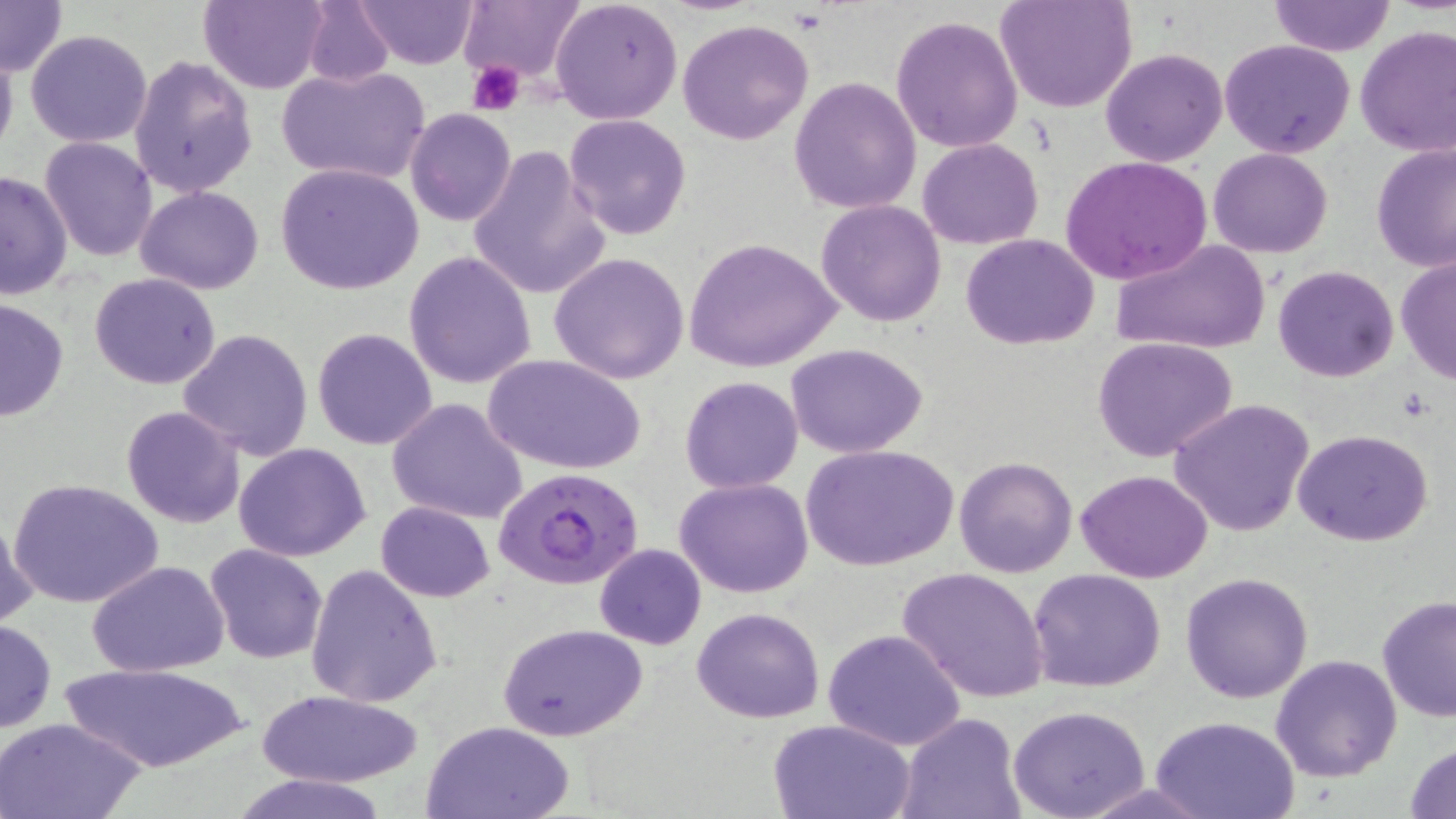

Summary:
  - Coordinate format: approximate bounding boxes as named x1/y1/x2/y2 corners in pixels
  - Uninfected red blood cell locations: (x1=0, y1=0, x2=67, y2=75), (x1=201, y1=0, x2=328, y2=94), (x1=355, y1=0, x2=478, y2=68), (x1=550, y1=0, x2=683, y2=125), (x1=996, y1=0, x2=1136, y2=113), (x1=1269, y1=0, x2=1394, y2=56), (x1=301, y1=2, x2=395, y2=90), (x1=459, y1=2, x2=583, y2=86), (x1=889, y1=15, x2=1025, y2=155), (x1=678, y1=19, x2=813, y2=144), (x1=1355, y1=25, x2=1456, y2=159), (x1=26, y1=29, x2=154, y2=147), (x1=1220, y1=38, x2=1355, y2=157), (x1=0, y1=41, x2=18, y2=163), (x1=1101, y1=48, x2=1227, y2=166), (x1=129, y1=55, x2=257, y2=197), (x1=279, y1=64, x2=431, y2=186), (x1=790, y1=75, x2=922, y2=215), (x1=406, y1=108, x2=515, y2=226), (x1=562, y1=114, x2=691, y2=241), (x1=40, y1=137, x2=157, y2=261), (x1=918, y1=138, x2=1044, y2=249), (x1=1370, y1=141, x2=1456, y2=271), (x1=466, y1=145, x2=609, y2=299), (x1=1208, y1=148, x2=1333, y2=259), (x1=1061, y1=155, x2=1212, y2=284), (x1=276, y1=163, x2=423, y2=294), (x1=0, y1=168, x2=72, y2=301), (x1=136, y1=186, x2=264, y2=294), (x1=816, y1=199, x2=948, y2=327), (x1=961, y1=233, x2=1099, y2=350), (x1=685, y1=238, x2=842, y2=371), (x1=1111, y1=239, x2=1272, y2=357), (x1=404, y1=251, x2=537, y2=390), (x1=549, y1=252, x2=690, y2=383), (x1=1394, y1=255, x2=1456, y2=383), (x1=1272, y1=265, x2=1399, y2=382), (x1=90, y1=273, x2=221, y2=389), (x1=0, y1=297, x2=68, y2=423), (x1=312, y1=327, x2=438, y2=449), (x1=178, y1=329, x2=314, y2=461), (x1=1092, y1=336, x2=1242, y2=464), (x1=786, y1=343, x2=928, y2=457), (x1=483, y1=354, x2=645, y2=476), (x1=681, y1=375, x2=802, y2=492), (x1=387, y1=398, x2=530, y2=525), (x1=1169, y1=398, x2=1315, y2=539), (x1=122, y1=405, x2=245, y2=528), (x1=1294, y1=428, x2=1433, y2=547), (x1=233, y1=443, x2=371, y2=563), (x1=804, y1=444, x2=958, y2=572), (x1=953, y1=455, x2=1078, y2=578), (x1=1075, y1=468, x2=1212, y2=583), (x1=675, y1=477, x2=814, y2=598), (x1=10, y1=478, x2=163, y2=610), (x1=375, y1=500, x2=496, y2=602), (x1=0, y1=511, x2=37, y2=634), (x1=593, y1=544, x2=707, y2=649), (x1=205, y1=545, x2=327, y2=663), (x1=88, y1=562, x2=229, y2=677), (x1=305, y1=564, x2=443, y2=707), (x1=897, y1=566, x2=1050, y2=702), (x1=1028, y1=568, x2=1168, y2=693), (x1=1180, y1=571, x2=1314, y2=704), (x1=1377, y1=594, x2=1456, y2=722), (x1=691, y1=607, x2=826, y2=724), (x1=0, y1=619, x2=56, y2=733), (x1=497, y1=623, x2=648, y2=741), (x1=824, y1=628, x2=967, y2=751), (x1=1270, y1=653, x2=1402, y2=782), (x1=59, y1=659, x2=249, y2=771), (x1=256, y1=690, x2=425, y2=787), (x1=1009, y1=706, x2=1150, y2=819), (x1=899, y1=713, x2=1024, y2=818), (x1=1152, y1=715, x2=1299, y2=819), (x1=0, y1=716, x2=146, y2=819), (x1=768, y1=717, x2=918, y2=819), (x1=424, y1=719, x2=576, y2=818), (x1=1406, y1=740, x2=1456, y2=818), (x1=230, y1=771, x2=391, y2=819)
  - Plasmodium falciparum-infected red blood cell locations: (x1=493, y1=467, x2=646, y2=592)
  - Platelet locations: (x1=470, y1=63, x2=523, y2=114)
  - Slide-level diagnosis: Plasmodium falciparum
  - Field of view: single
  - Preparation: thin blood smear
  - Image size: 1456×819 pixels
  - Stain: May-Grünwald-Giemsa
  - Magnification: 1000x
  - Modality: optical microscopy